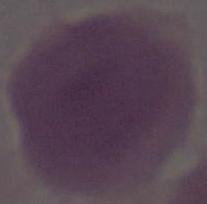 1000x magnification. An erythrocyte is seen. Micrograph.